Locate and identify every blood parasite.
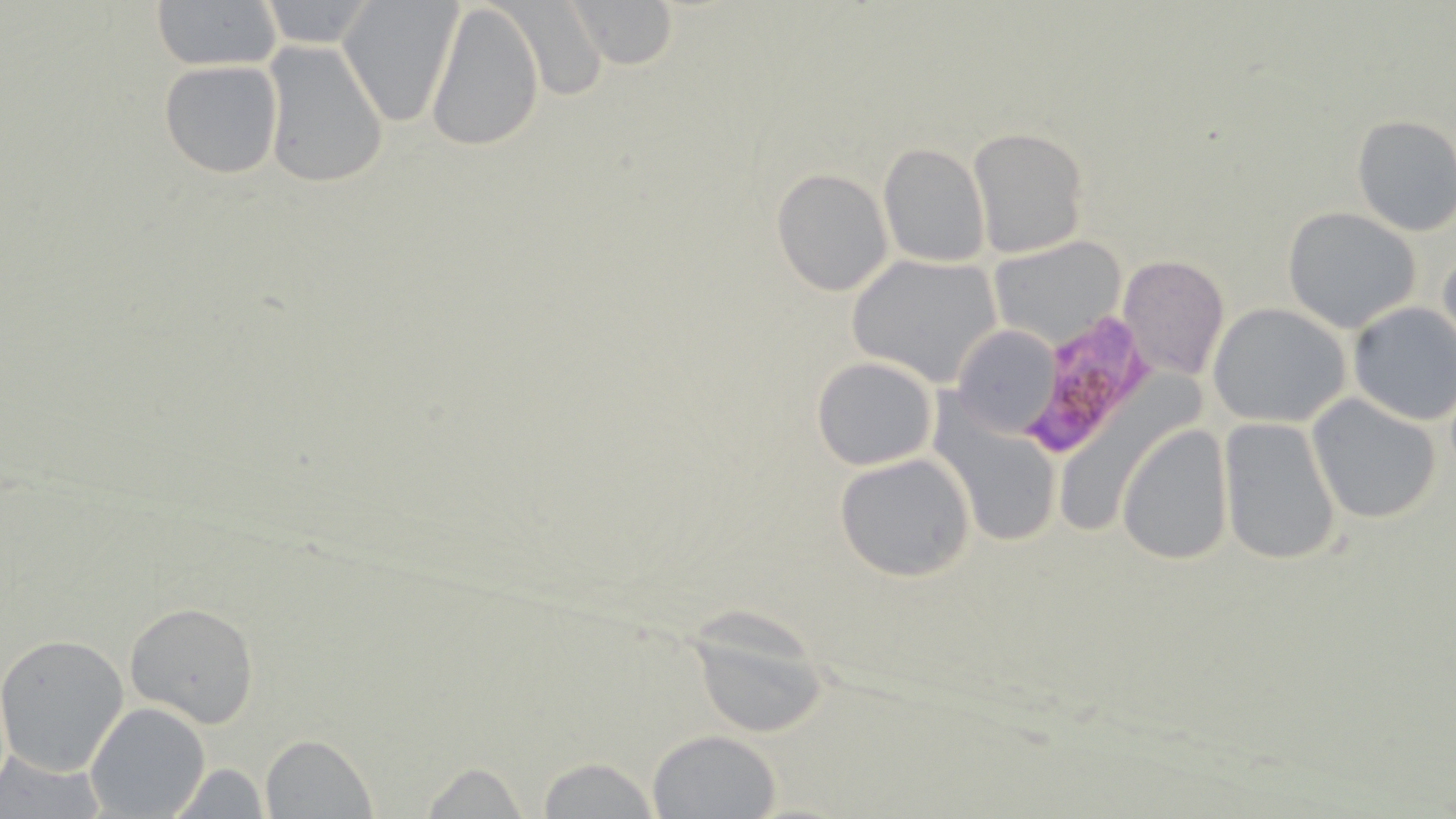

Approximate bounding boxes as (x1,y1)-(x2,y2) corner pairs in pixels.
Plasmodium falciparum-infected red blood cells: (1023,312)-(1157,461).
No Plasmodium ovale, Plasmodium malariae, Plasmodium vivax, Babesia divergens, or Trypanosoma brucei observed.

Uninfected red blood cell locations: (148,0)-(286,70), (336,0)-(464,129), (424,0)-(545,154), (496,0)-(611,101), (562,0)-(679,69), (253,1)-(381,50), (259,40)-(390,189), (158,58)-(284,178), (1350,114)-(1456,237), (967,126)-(1090,258), (878,142)-(992,266), (772,168)-(893,295), (1283,207)-(1422,333), (990,235)-(1129,348), (1438,240)-(1456,365), (1117,253)-(1229,382), (847,255)-(1002,387), (1347,301)-(1456,425), (1207,302)-(1352,426), (952,326)-(1062,438), (811,355)-(939,471), (1306,395)-(1443,524), (939,411)-(1066,549), (1217,418)-(1342,566), (1117,426)-(1234,564), (833,452)-(977,582), (122,601)-(261,730), (681,607)-(830,739), (0,635)-(130,776), (86,701)-(211,819), (648,730)-(781,817), (260,734)-(376,817), (0,750)-(105,819), (536,755)-(662,819), (417,760)-(531,819), (164,762)-(272,817). Slide-level diagnosis: Plasmodium falciparum. Single field of view. Optical microscopy. Image is 1456×819 pixels. Thin blood smear. 1000x magnification. May-Grünwald-Giemsa-stained preparation.